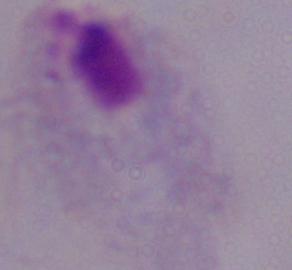

Micrograph. Captured at 1000x magnification. A trichomonad is seen.